Comment on the morphology of the erythrocytes.
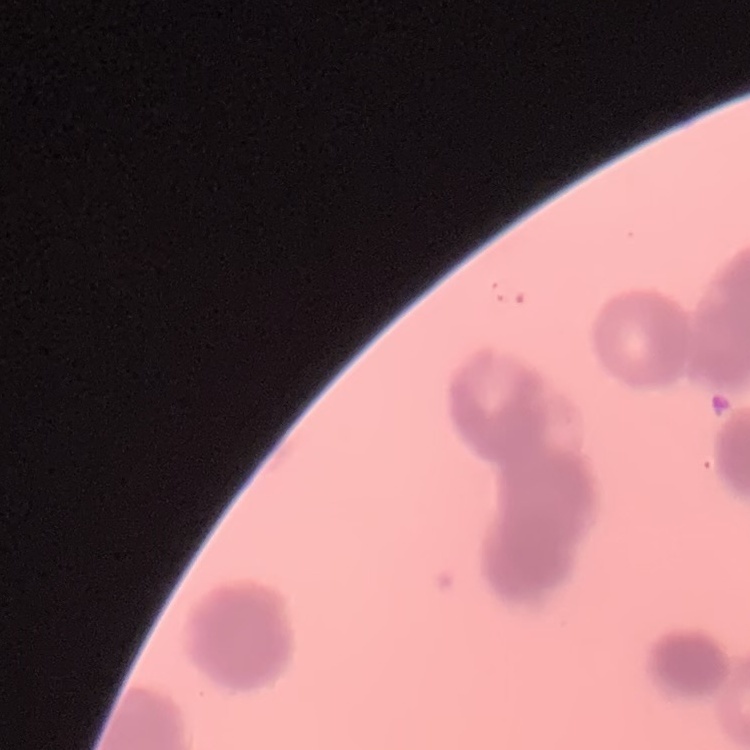
Rouleaux formation.

Square crop of a larger photomicrograph. Stained with either Field's or Giemsa. Thin blood smear.